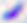
magnification = 400x
modality = photomicrograph
identification = Toxoplasma gondii